Locate every Plasmodium ovale-infected red blood cell.
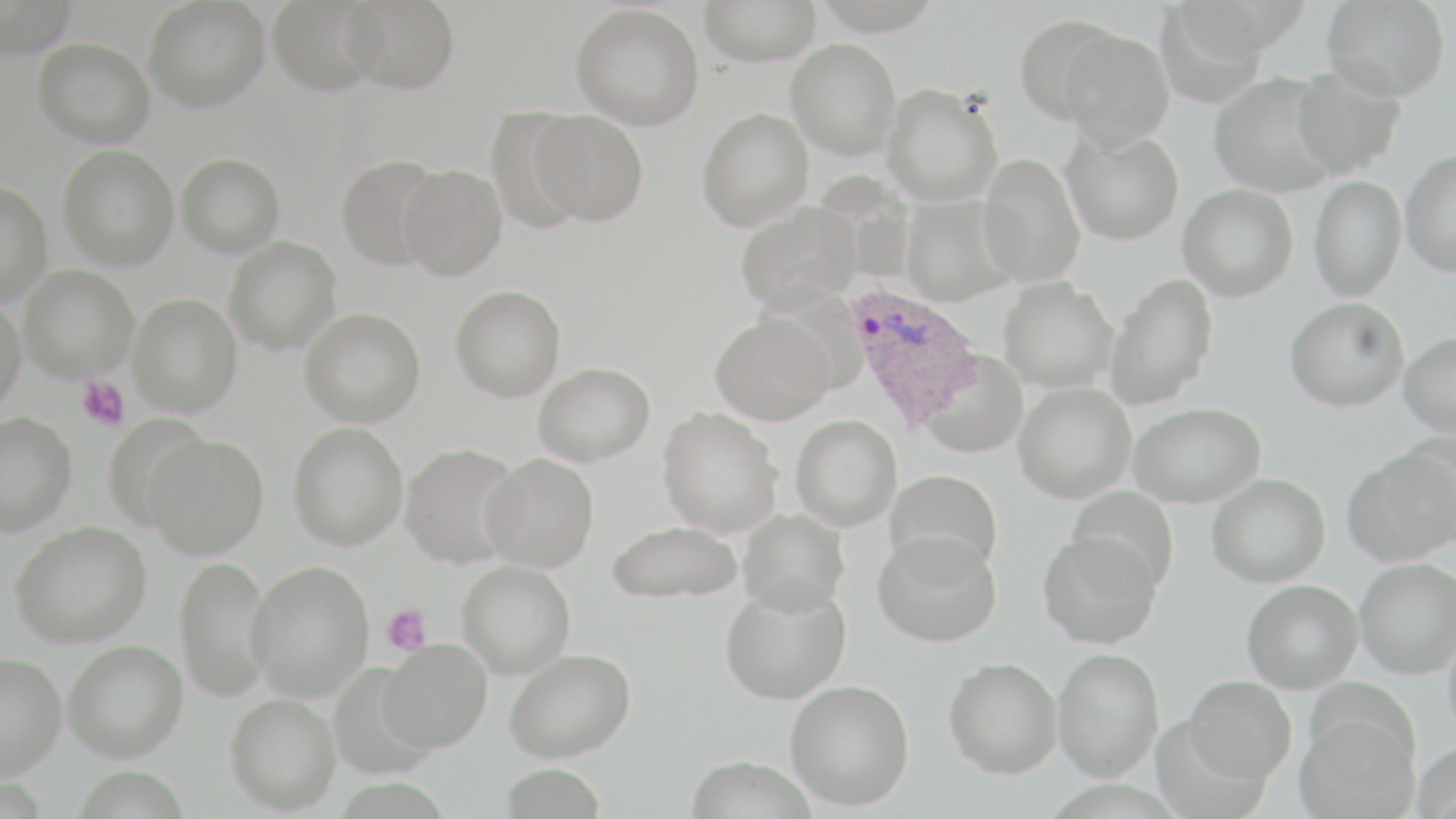
Approximate bounding boxes as [x1, y1, x2, y2] in pixels.
Plasmodium ovale-infected red blood cells: [843, 281, 984, 433].

Uninfected red blood cell locations: [0, 0, 77, 58], [143, 0, 270, 111], [268, 0, 382, 96], [340, 0, 459, 94], [812, 0, 945, 35], [1174, 0, 1312, 60], [1321, 0, 1451, 100], [698, 1, 820, 65], [570, 3, 704, 130], [1154, 3, 1280, 103], [1014, 14, 1123, 123], [1058, 27, 1174, 146], [32, 38, 155, 147], [786, 38, 902, 159], [1290, 65, 1407, 178], [1209, 72, 1342, 197], [881, 83, 1004, 206], [696, 107, 814, 231], [527, 109, 648, 225], [1062, 128, 1184, 244], [57, 144, 178, 270], [1399, 148, 1456, 277], [176, 152, 286, 257], [977, 152, 1085, 288], [336, 154, 447, 270], [396, 164, 507, 280], [1309, 175, 1406, 301], [0, 178, 53, 307], [1177, 183, 1298, 301], [900, 194, 1016, 306], [734, 201, 859, 314], [224, 236, 342, 354], [18, 264, 139, 381], [1105, 274, 1218, 409], [999, 277, 1119, 393], [449, 284, 566, 401], [128, 293, 242, 416], [0, 296, 27, 416], [1285, 296, 1410, 411], [298, 307, 426, 427], [709, 312, 836, 426], [1399, 332, 1456, 438], [921, 351, 1029, 457], [532, 362, 655, 466], [1013, 382, 1136, 503], [1128, 402, 1266, 507], [656, 406, 783, 538], [0, 411, 77, 535], [791, 414, 903, 531], [101, 415, 214, 528], [287, 422, 409, 550], [144, 434, 268, 558], [399, 442, 523, 568], [1343, 449, 1455, 566], [479, 453, 600, 571], [884, 469, 1003, 575], [1207, 473, 1330, 587], [1067, 485, 1181, 592], [737, 508, 850, 615], [606, 519, 743, 605], [8, 521, 151, 647], [1037, 530, 1162, 649], [873, 531, 1002, 647], [174, 555, 274, 701], [1355, 558, 1456, 678], [246, 560, 374, 701], [457, 560, 576, 678], [1242, 579, 1363, 693], [720, 584, 851, 704], [1443, 624, 1456, 745], [378, 639, 492, 752], [62, 640, 188, 761], [1053, 647, 1164, 781], [504, 648, 636, 762], [0, 651, 66, 778], [945, 657, 1062, 778], [1184, 675, 1297, 783], [785, 679, 914, 810], [225, 692, 341, 813], [1295, 711, 1419, 819], [1412, 741, 1456, 818], [685, 753, 819, 818], [499, 763, 608, 819]. Platelet locations: [76, 376, 131, 431], [382, 605, 432, 655]. Slide-level diagnosis: Plasmodium ovale. Captured at 1000x magnification. Light microscopy. Image is 1456×819 pixels. Single field of view. May-Grünwald-Giemsa-stained preparation. Thin blood film.